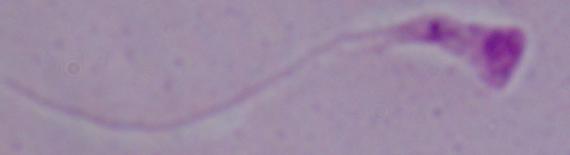
Summary:
  - Modality: micrograph
  - Identification: Leishmania
  - Magnification: 1000x